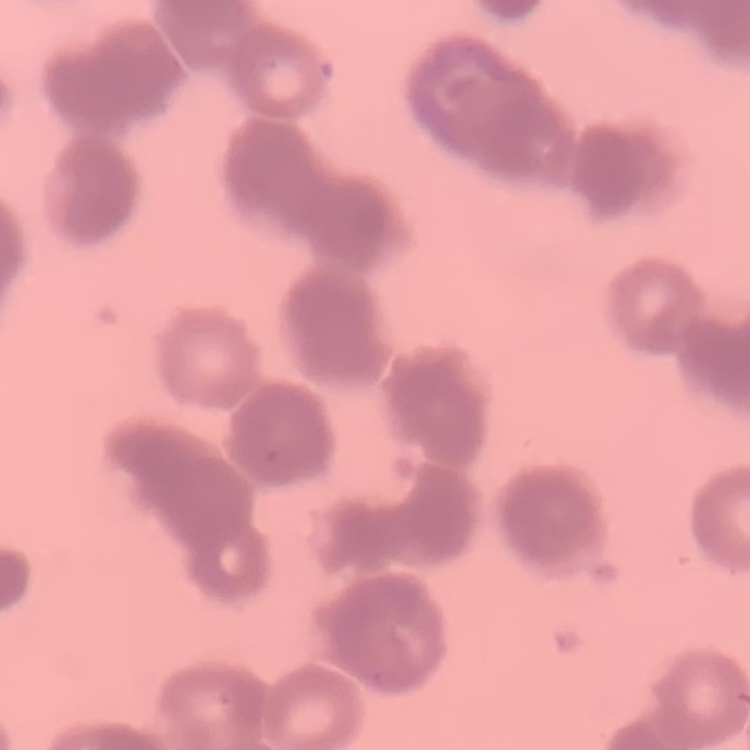

Summary:
  - Erythrocyte morphology: rouleaux formation
  - Stain: Field's or Giemsa
  - Image type: one tile cut from a larger photomicrograph
  - Preparation: thin blood smear